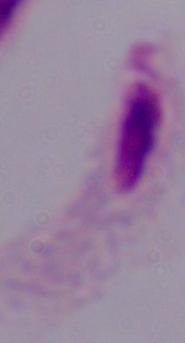
Micrograph. A trichomonad is shown. Captured at 1000x magnification.